Report the malaria status of this cell.
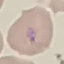
It is parasitized.

preparation: thin smear
capture: smartphone through the microscope eyepiece
image_type: cell patch, automatically extracted from a larger field of view and resized to 64 × 64 pixels
stain: Giemsa